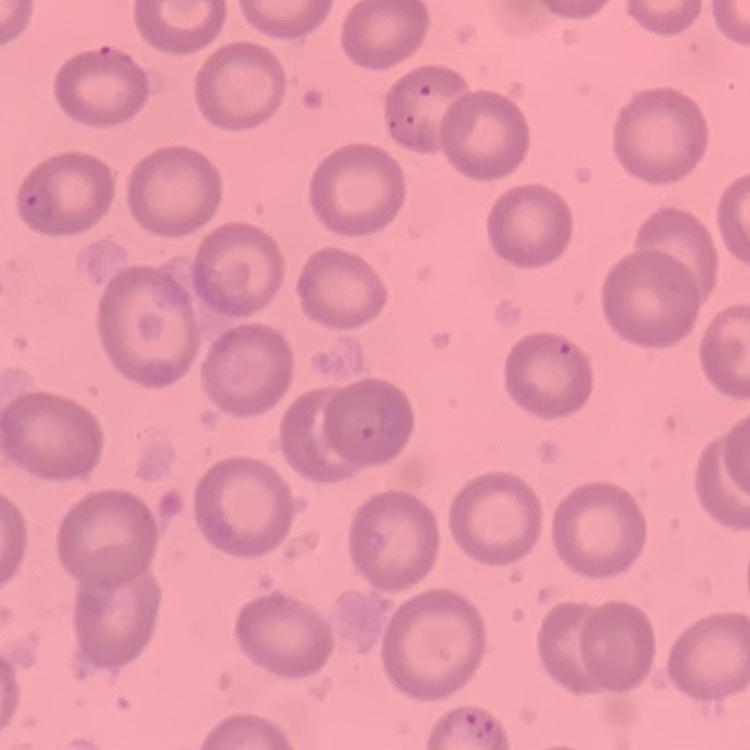
erythrocyte morphology = no rouleaux formation
stain = Field's or Giemsa
preparation = thin blood smear
image type = square crop of a larger photomicrograph